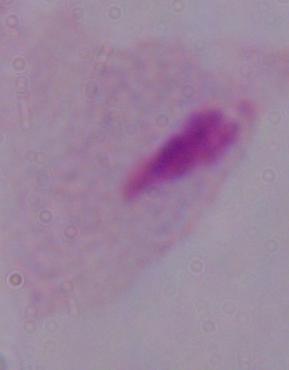
Summary:
  - Magnification: 1000x
  - Modality: photomicrograph
  - Identification: trichomonad